Name the parasite shown.
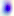
Toxoplasma gondii.

Summary:
  - Modality: photomicrograph
  - Magnification: 400x